Assess this cell for malaria.
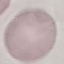

It is uninfected.

Giemsa stain. Cell patch, automatically extracted from a larger field of view and resized to 64 × 64 pixels. Thin blood film. Acquired by smartphone through the microscope eyepiece.